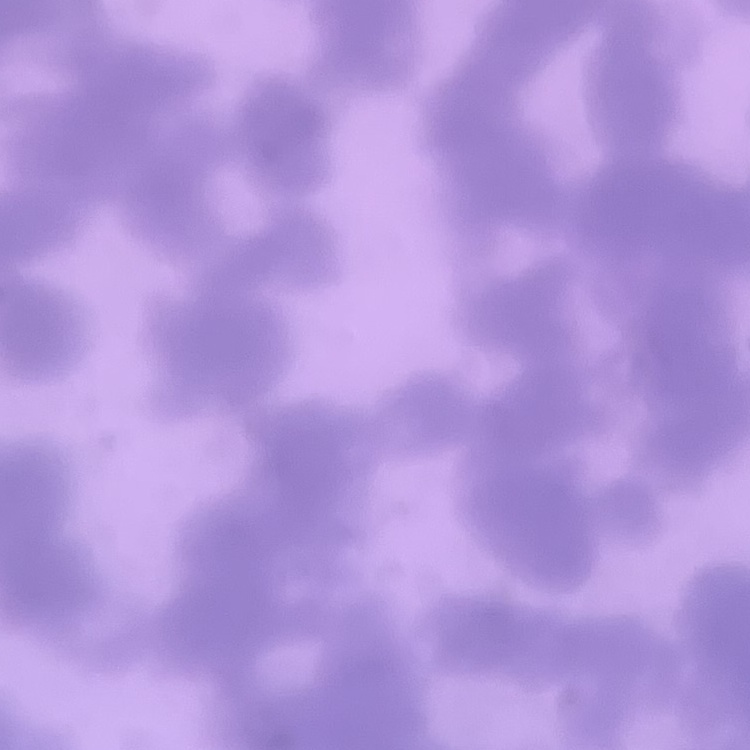

red_blood_cell_morphology: rouleaux formation
image_type: square crop of a larger photomicrograph
stain: Field's or Giemsa
preparation: thin blood smear